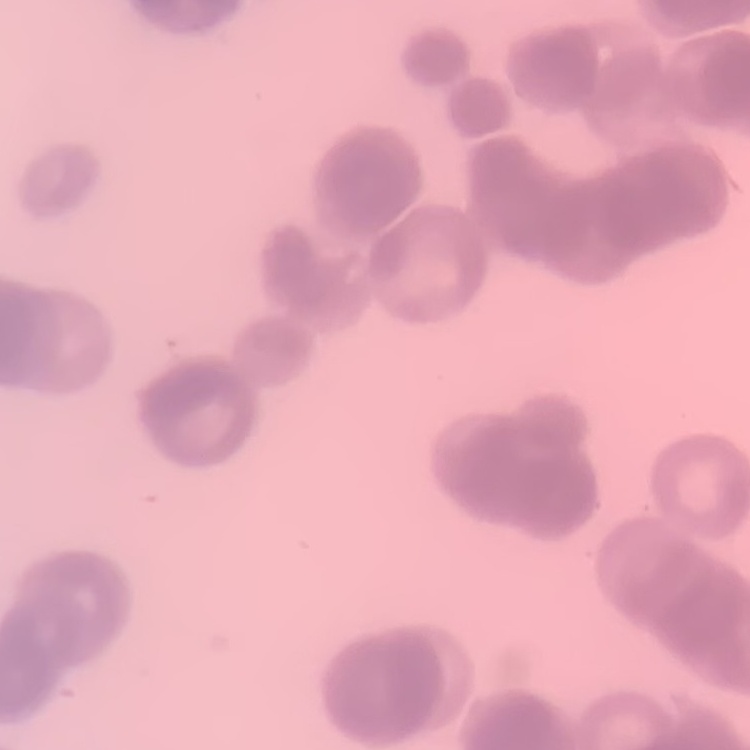
The red blood cells exhibit rouleaux formation. Field's or Giemsa stain. Thin blood film. One tile cut from a larger photomicrograph.